Report the malaria status of this cell.
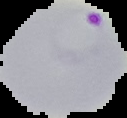
Parasitized.

image size = 127×118 pixels
preparation = thin blood smear
image type = segmented cell region on a black background